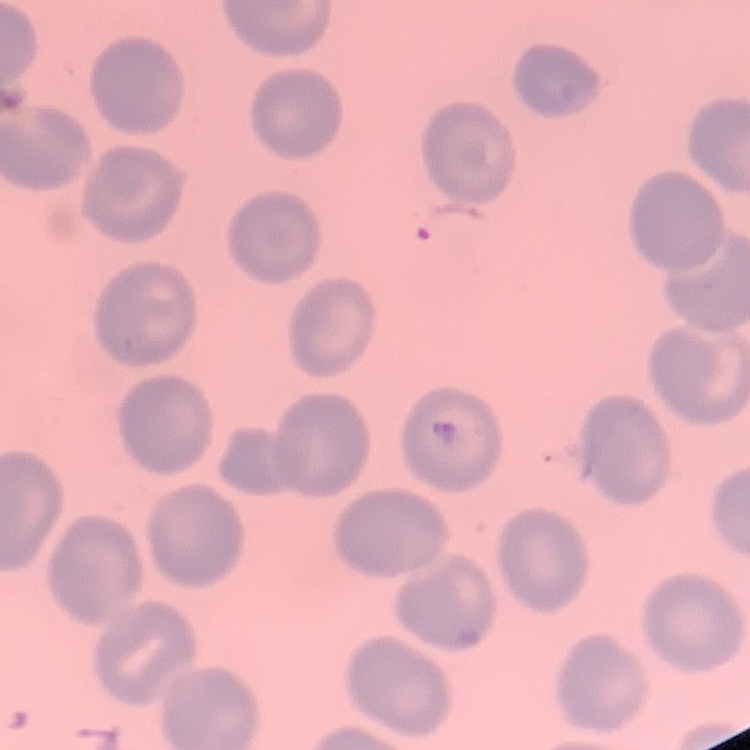
Summary:
  - Red blood cell morphology: no rouleaux formation
  - Image type: one tile cut from a larger photomicrograph
  - Preparation: thin blood film
  - Stain: Field's or Giemsa